Assess this cell for malaria.
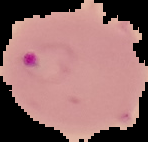
It is parasitized.

image type = segmented cell region with the area outside set to black
preparation = thin blood smear
image size = 148×142 pixels